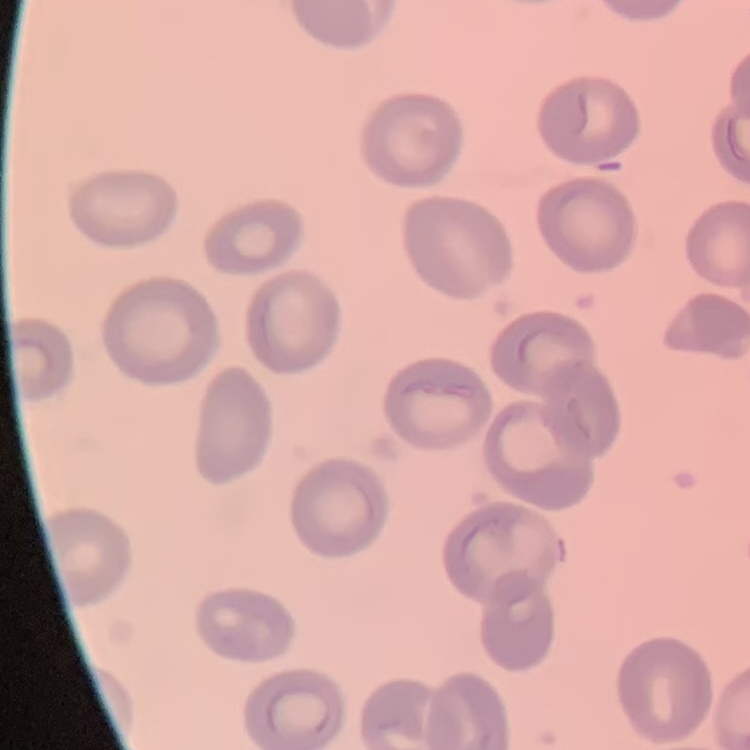
erythrocyte morphology = no rouleaux formation
image type = square crop of a larger photomicrograph
preparation = thin blood smear
stain = Field's or Giemsa